Describe the morphology of the red blood cells.
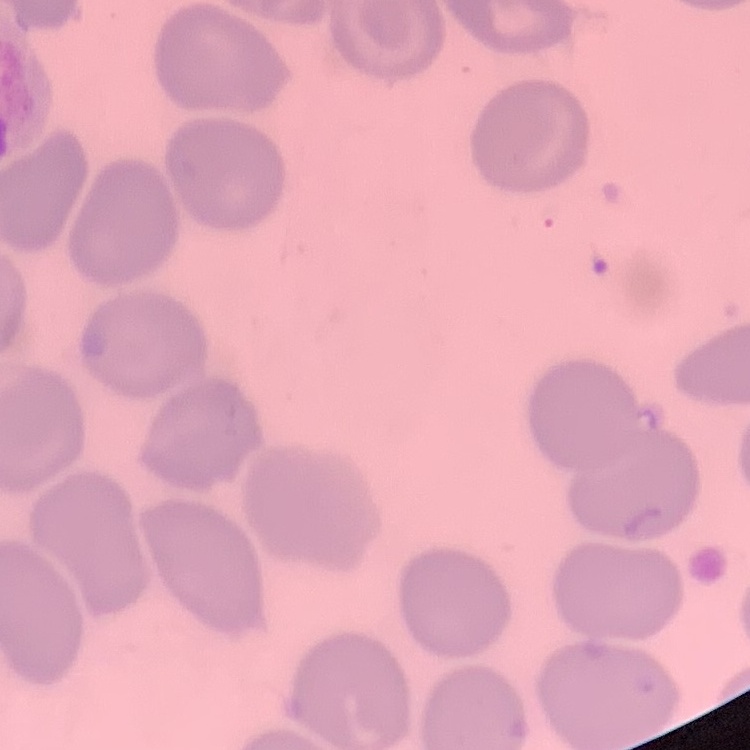
No rouleaux formation.

Summary:
  - Preparation: thin peripheral smear
  - Stain: Field's or Giemsa
  - Image type: square crop of a larger photomicrograph